State which cell type is depicted.
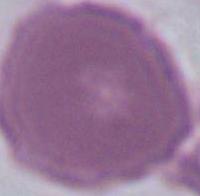

This is an erythrocyte.

Micrograph. 1000x magnification.